Report the malaria status of this cell.
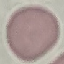
It is uninfected.

stain = Giemsa
image type = automatically extracted cell patch, resized to 64 × 64 pixels
capture = smartphone through the microscope eyepiece
preparation = thin blood film